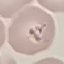

Summary:
  - Malaria status: parasitized
  - Image type: cell patch, automatically extracted from a larger field of view and resized to 64 × 64 pixels
  - Capture: smartphone through the microscope eyepiece
  - Stain: Giemsa
  - Preparation: thin blood smear